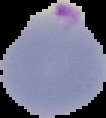
Summary:
  - Preparation: thin blood film
  - Result: Plasmodium parasites detected
  - Image size: 106×118 pixels
  - Image type: segmented cell region on a black background